Describe the morphology of the red blood cells.
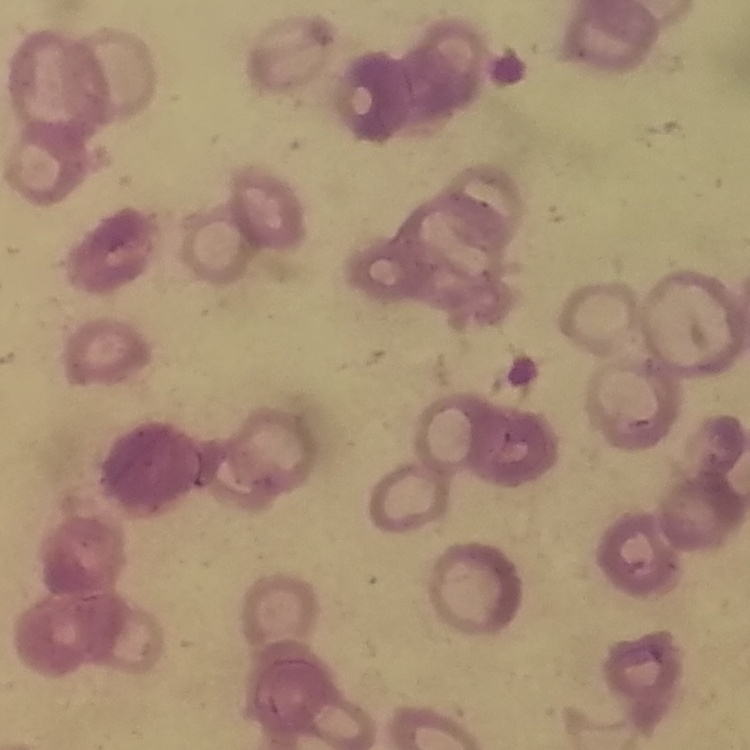
They show rouleaux formation.

Summary:
  - Stain: Field's or Giemsa
  - Preparation: thin blood film
  - Image type: square crop of a larger photomicrograph